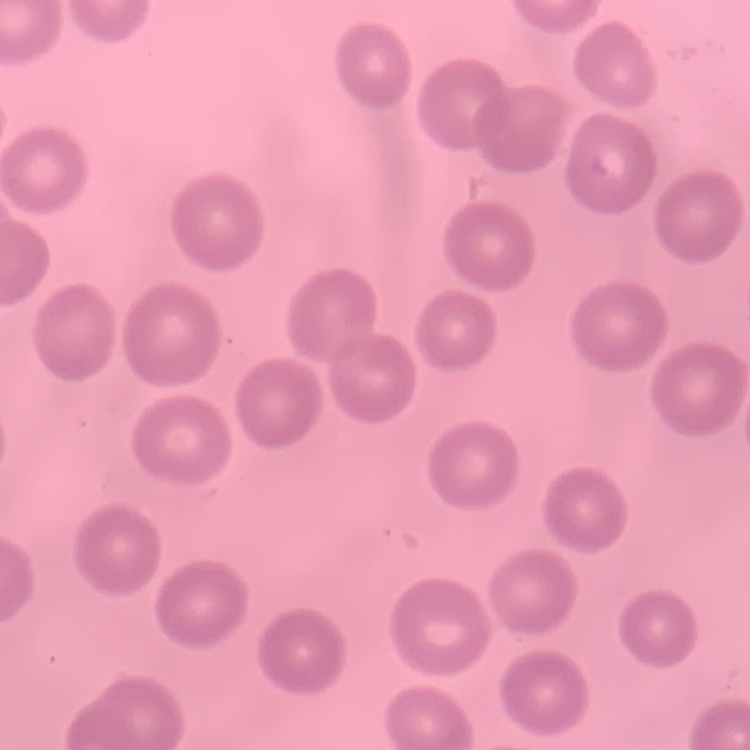
red blood cell morphology = no rouleaux formation
image type = one tile cut from a larger photomicrograph
stain = Field's or Giemsa
preparation = thin peripheral smear